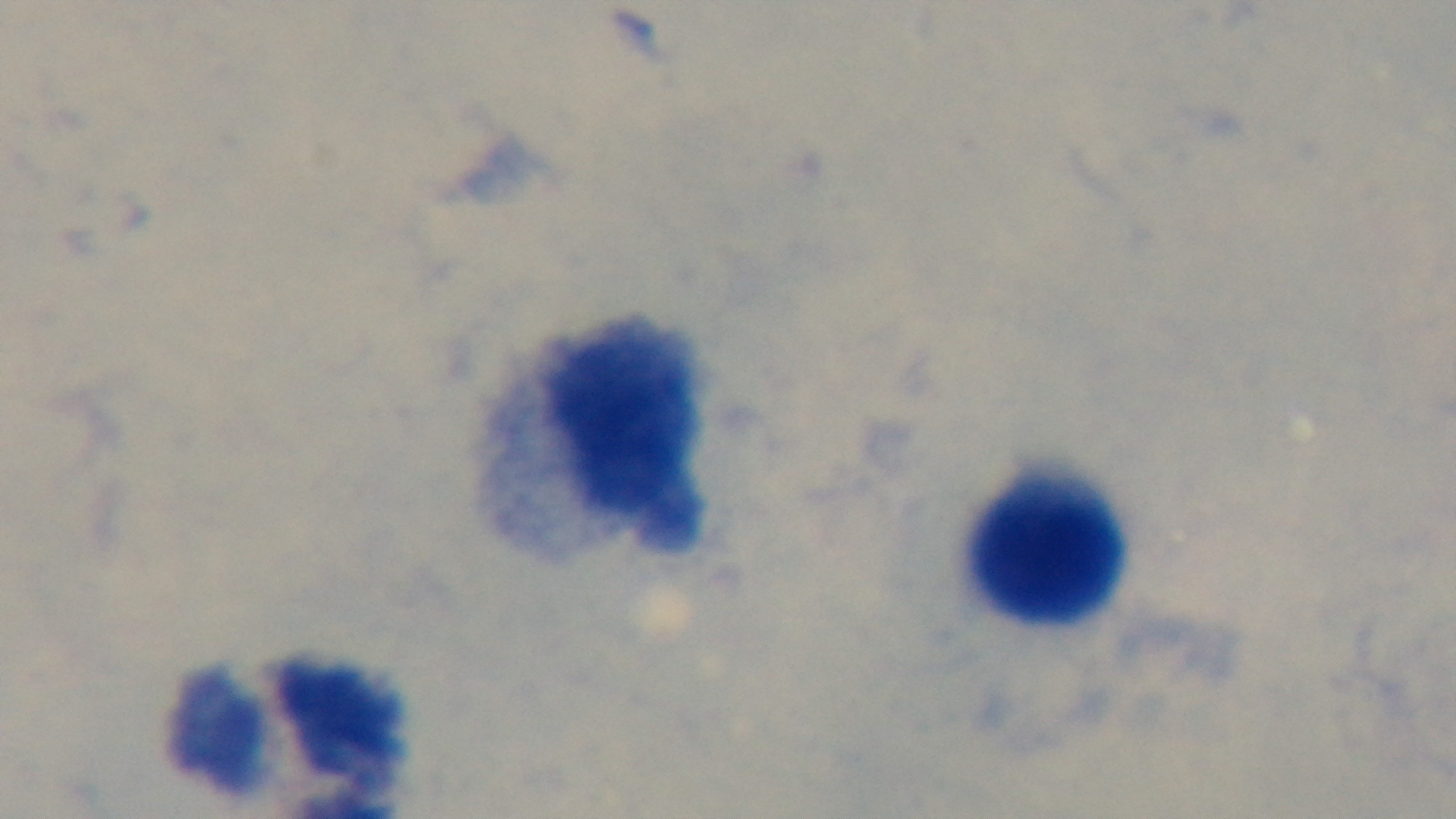
stain = Giemsa
field of view = single
preparation = thick blood film
malaria status = negative
objective = 100x oil immersion
modality = light microscopy
capture = mounted 4K digital camera